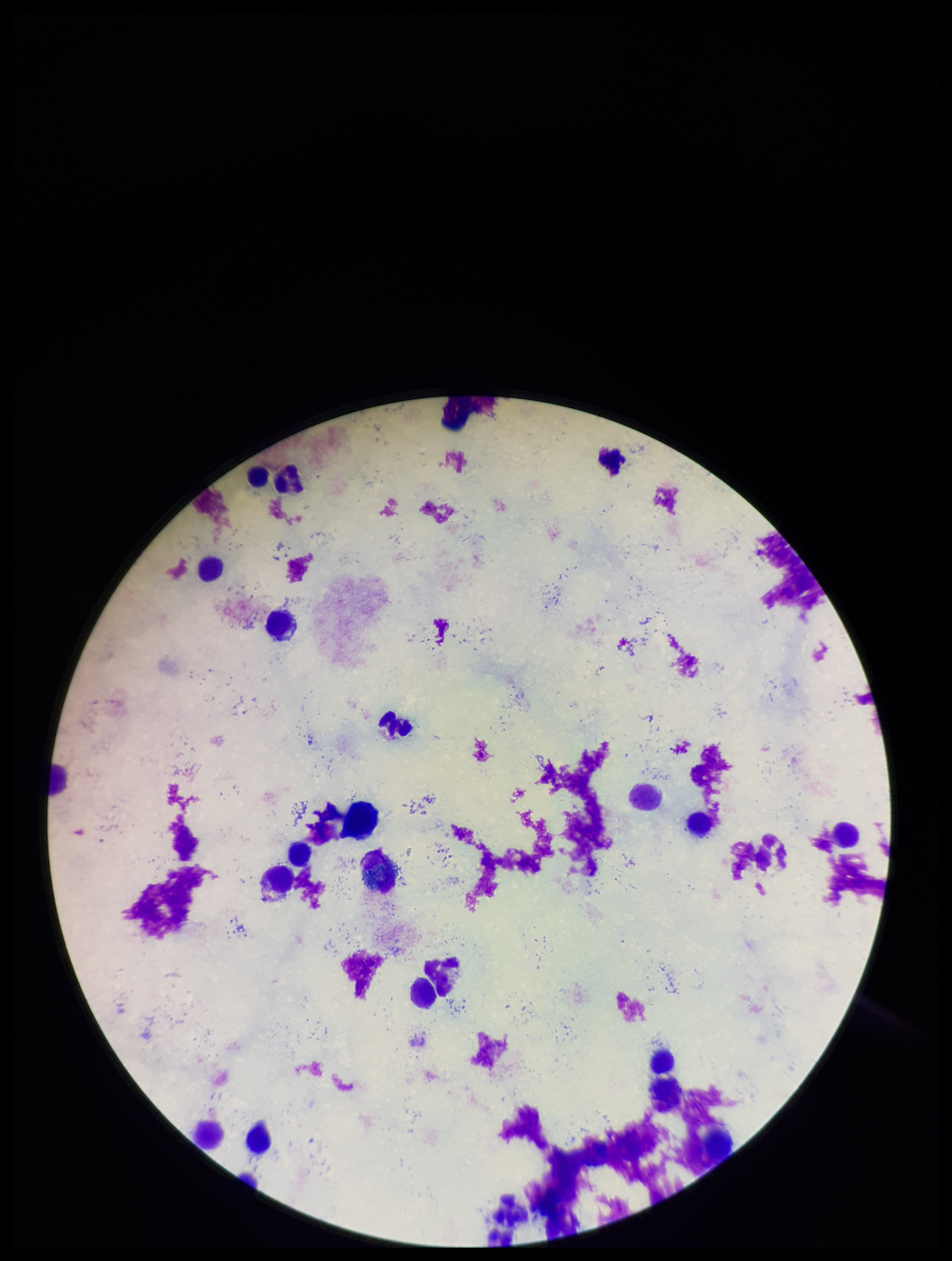

Preparation: thick. Plasmodium parasites: none seen. Smartphone photograph taken through the eyepiece of a microscope. Image is 952×1261 pixels. Patient malaria status: negative. Parasite count: 0. Leukocyte count: 23. Stained with Giemsa. One field from this slide.